Assess this cell for malaria.
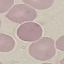
It is uninfected.

Summary:
  - Stain: Giemsa
  - Capture: smartphone through the microscope eyepiece
  - Preparation: thin blood smear
  - Image type: cell patch, automatically extracted from a larger field of view and resized to 64 × 64 pixels